Assess this cell for malaria.
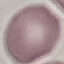

It is uninfected.

Acquired by smartphone through the microscope eyepiece. Cell patch, automatically extracted from a larger field of view and resized to 64 × 64 pixels. Giemsa stain. Thin blood film.